Evaluate for malaria.
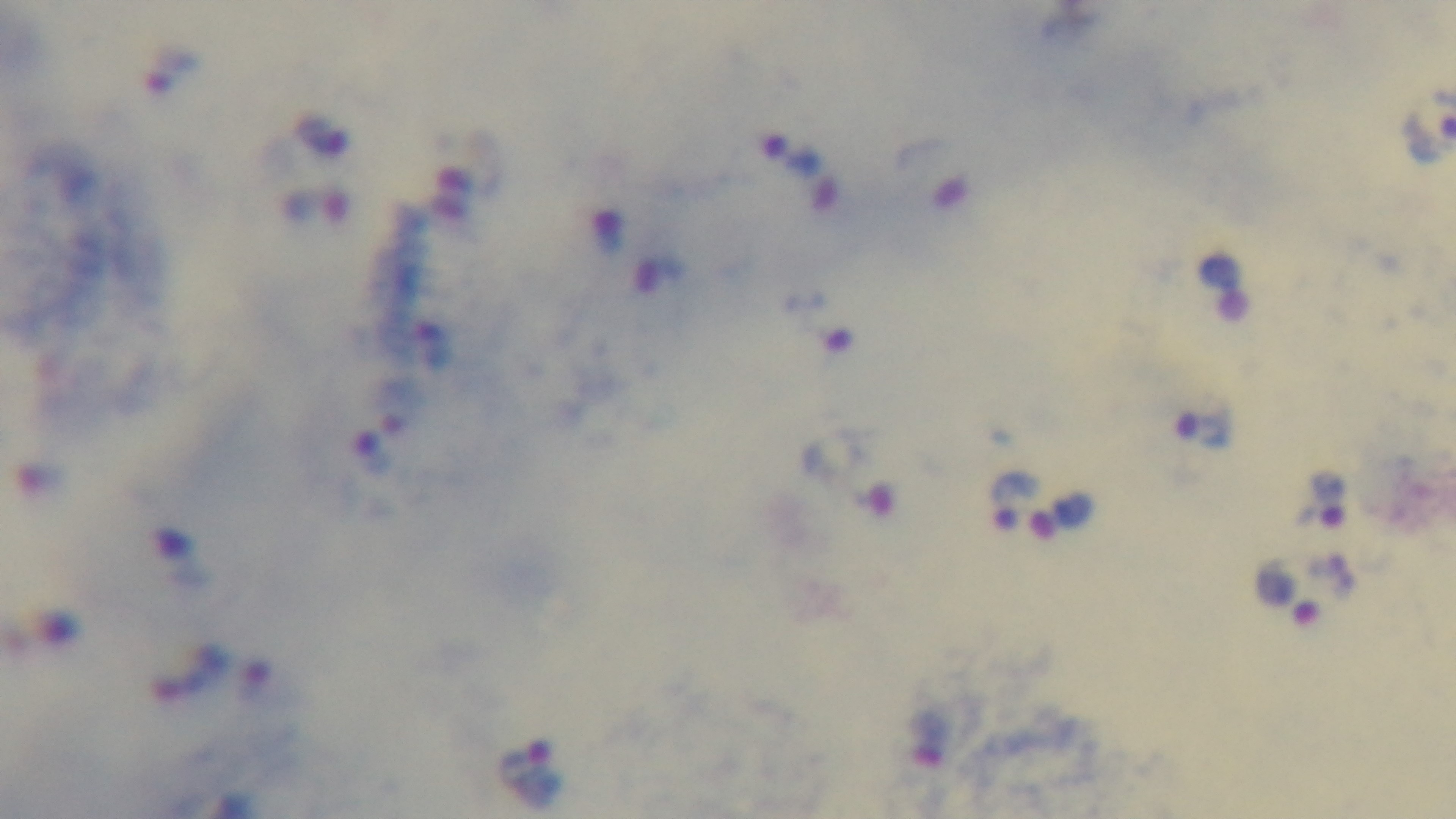

It is infected.

field of view = one from the slide
preparation = thick
stain = Giemsa
capture = mounted 4K digital camera
objective = 100x oil immersion
modality = light microscopy